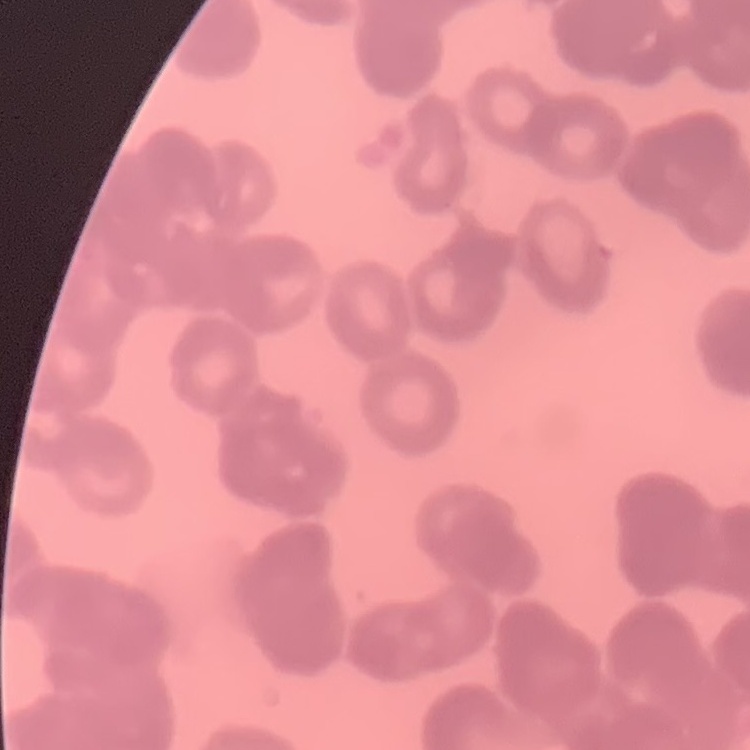
Summary:
  - Erythrocyte morphology: rouleaux formation
  - Preparation: thin blood smear
  - Stain: Field's or Giemsa
  - Image type: one tile cut from a larger photomicrograph